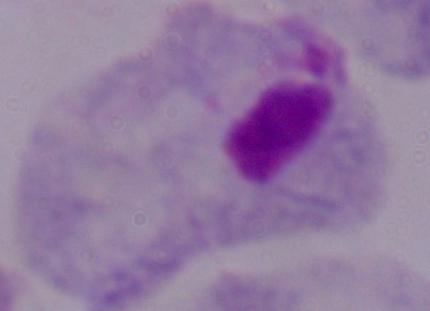
modality: micrograph
identification: trichomonad
magnification: 1000x